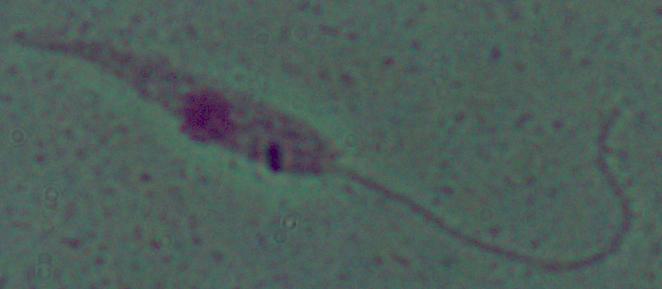
identification = Leishmania
modality = photomicrograph
magnification = 1000x